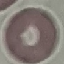

Malaria status: uninfected. Acquired by smartphone through the microscope eyepiece. Automatically extracted cell patch, resized to 64 × 64 pixels. Thin blood smear. Giemsa-stained preparation.